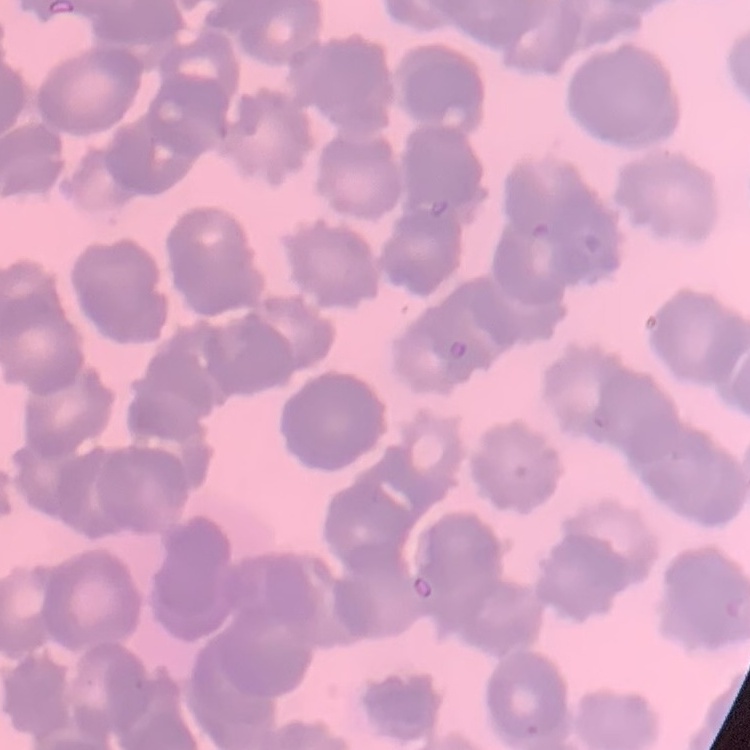

red blood cell morphology = rouleaux formation
image type = square crop of a larger photomicrograph
preparation = thin blood film
stain = Field's or Giemsa